Identify the parasite.
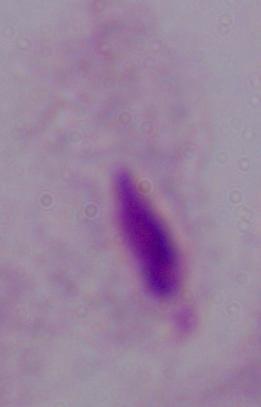
A trichomonad.

modality = photomicrograph
magnification = 1000x